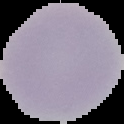
preparation: thin blood smear
result: no Plasmodium parasites seen
image_size: 124×124 pixels
image_type: segmented cell region with the area outside set to black